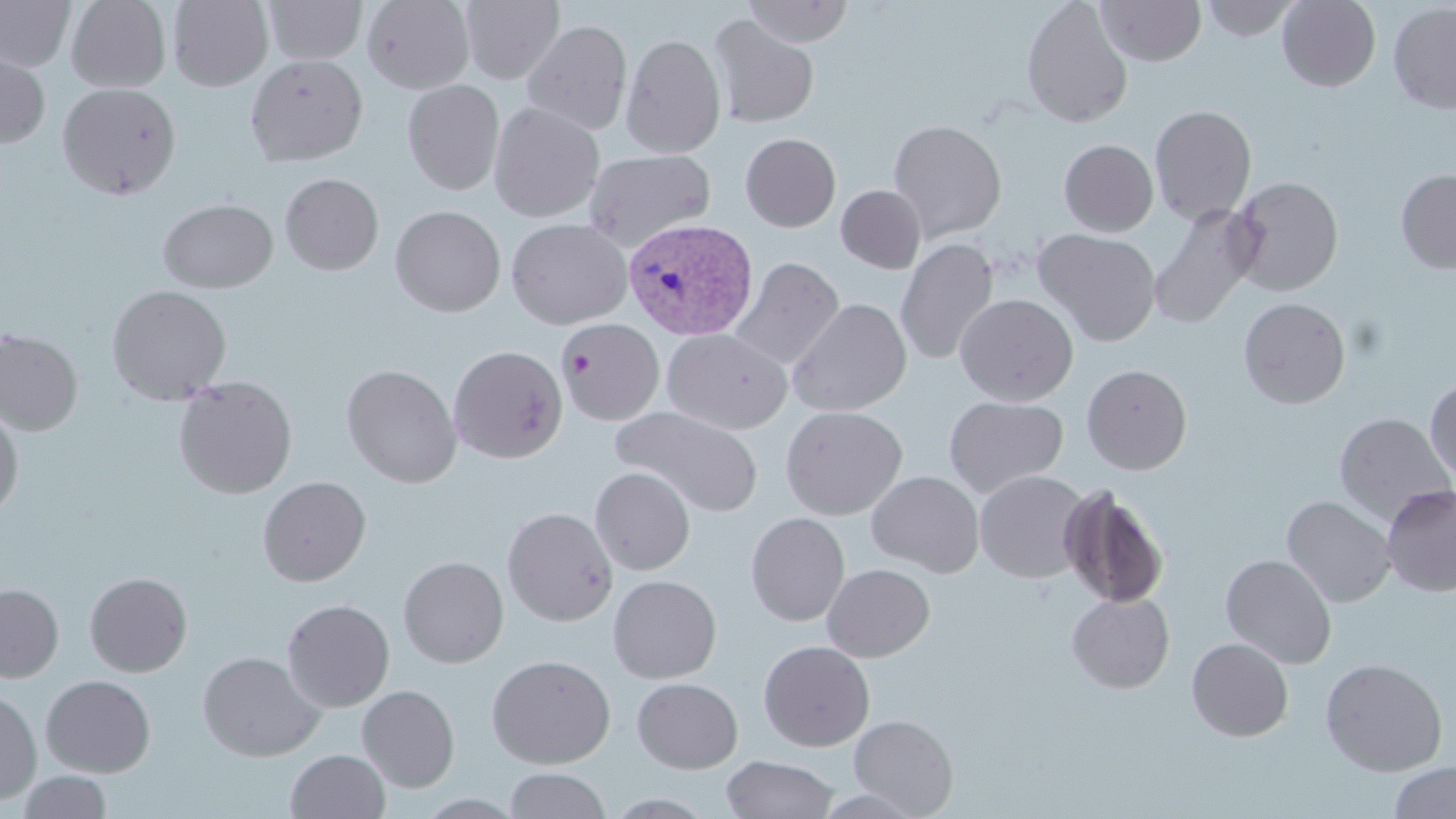 Approximate bounding boxes as (x1,y1)-(x2,y2) corner pairs in pixels. Platelet locations: (561,349)-(595,378). Uninfected red blood cell locations: (0,0)-(75,73), (66,0)-(171,92), (168,0)-(272,90), (264,0)-(367,65), (362,0)-(475,94), (459,0)-(564,84), (742,0)-(854,47), (1021,0)-(1133,128), (1096,0)-(1207,66), (1199,0)-(1301,42), (1277,0)-(1381,92), (1388,2)-(1456,115), (707,14)-(819,128), (521,19)-(632,135), (620,32)-(726,159), (0,47)-(51,149), (245,54)-(368,166), (402,79)-(504,196), (57,82)-(182,199), (488,101)-(605,222), (1149,104)-(1257,225), (888,119)-(1007,241), (740,133)-(841,232), (1058,139)-(1158,236), (583,148)-(716,251), (1395,169)-(1456,273), (280,173)-(384,275), (1228,176)-(1343,296), (836,185)-(926,273), (158,198)-(278,293), (1148,204)-(1262,329), (390,205)-(505,317), (506,217)-(632,329), (1033,229)-(1161,345), (895,238)-(999,365), (730,256)-(844,371), (106,284)-(232,405), (955,293)-(1078,406), (1239,297)-(1350,408), (788,298)-(912,417), (559,318)-(665,424), (662,328)-(792,434), (0,329)-(83,436), (448,344)-(568,463), (341,363)-(462,488), (1081,364)-(1192,474), (173,376)-(297,499), (1425,376)-(1456,485), (943,396)-(1069,497), (611,405)-(763,518), (780,405)-(907,520), (0,407)-(24,521), (1334,413)-(1455,525), (590,467)-(695,575), (866,470)-(984,577), (975,470)-(1090,582), (257,476)-(371,586), (1058,484)-(1169,608), (1381,485)-(1456,596), (1282,495)-(1397,608), (502,506)-(617,626), (746,512)-(850,626), (1220,553)-(1337,668), (398,556)-(509,667), (822,563)-(935,662), (85,572)-(193,677), (607,574)-(722,683), (0,583)-(64,682), (1066,592)-(1175,693), (282,599)-(395,712), (1187,637)-(1294,741), (758,640)-(875,752), (197,651)-(325,761), (486,654)-(616,769), (1320,657)-(1448,776), (41,674)-(155,777), (632,677)-(743,773), (357,685)-(459,792), (0,689)-(41,805), (849,714)-(958,817), (285,749)-(390,819), (721,755)-(838,818), (1388,761)-(1456,818), (504,768)-(611,819), (17,770)-(113,818), (813,787)-(928,819). Plasmodium vivax-infected red blood cell locations: (623,218)-(758,341). Slide-level diagnosis: Plasmodium vivax. May-Grünwald-Giemsa-stained preparation. Thin blood smear. One field of a larger specimen. 1000x magnification. Image is 1456×819 pixels. Light microscopy.